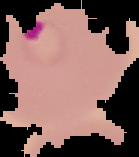

Image is 139×157 pixels. From a thin blood film. Result: malaria parasites detected. Segmented cell region on a black background.